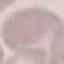

Malaria status: uninfected. Giemsa-stained preparation. Cell patch, automatically extracted from a larger field of view and resized to 64 × 64 pixels. Thin blood film. Photographed with a smartphone camera at the microscope eyepiece.